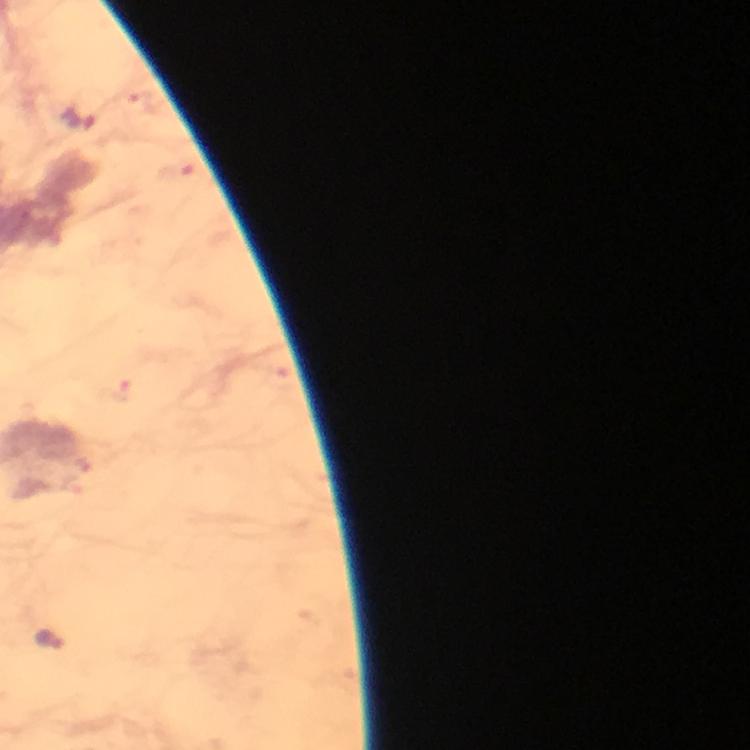
Approximate object centers, in pixels from the top-left corner.
Summary:
  - Malaria parasite locations: (x=79, y=120), (x=49, y=638)
  - Stain: Giemsa
  - Context: from a diagnostic examination for malaria
  - Immersion oil: used
  - Cropped from: one field of view
  - Image size: 750×750 pixels
  - Magnification: 100x
  - Preparation: thick blood smear
  - Capture: smartphone photograph through a microscope